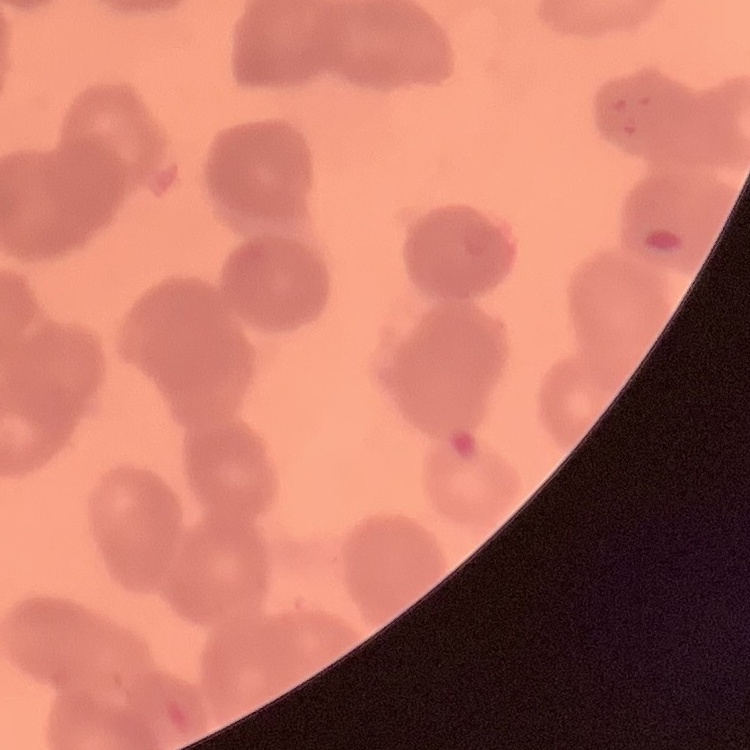

Summary:
  - Red blood cell morphology: rouleaux formation
  - Preparation: thin peripheral smear
  - Image type: square crop of a larger photomicrograph
  - Stain: Field's or Giemsa